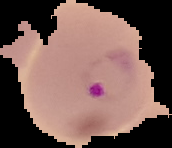 Image is 172×148 pixels. Malaria status: parasitized. Cell region segmented out of the field of view; the surrounding area is masked to black. From a thin blood film.